Comment on the morphology of the red blood cells.
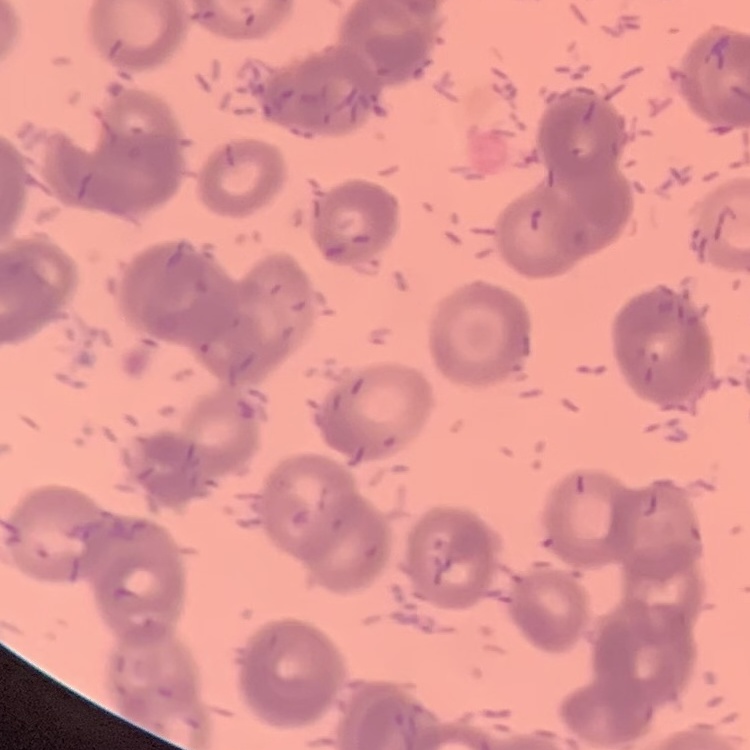

Rouleaux formation.

Stained with either Field's or Giemsa. Thin blood film. One tile cut from a larger photomicrograph.